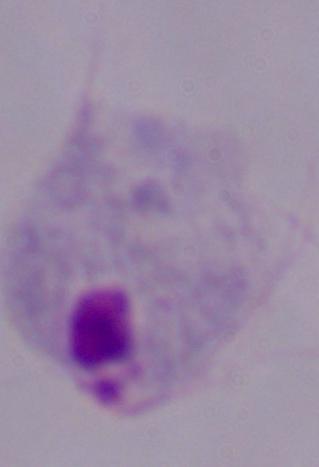

magnification: 1000x
identification: trichomonad
modality: micrograph